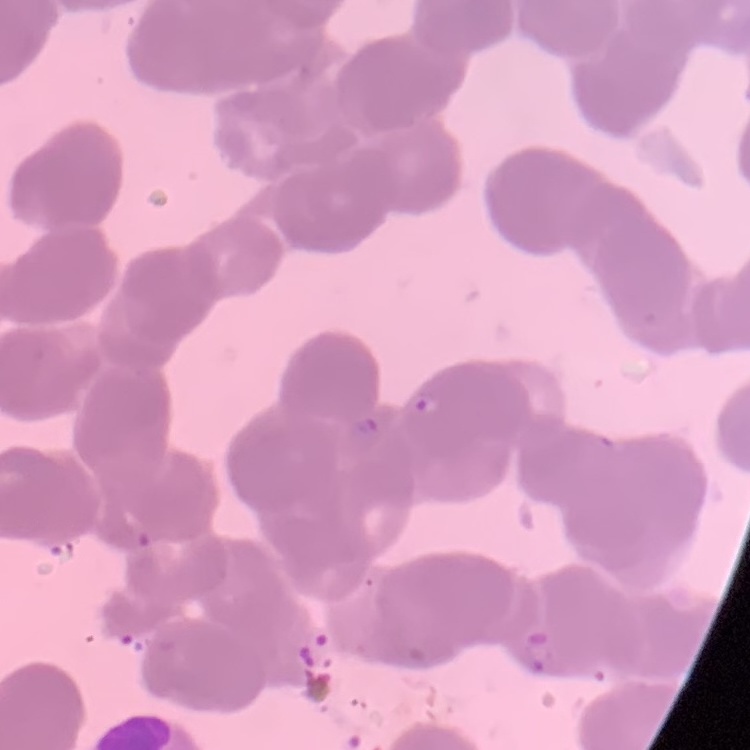
{
  "erythrocyte_morphology": "rouleaux formation",
  "preparation": "thin blood smear",
  "stain": "Field's or Giemsa",
  "image_type": "square crop of a larger photomicrograph"
}